Evaluate for malaria.
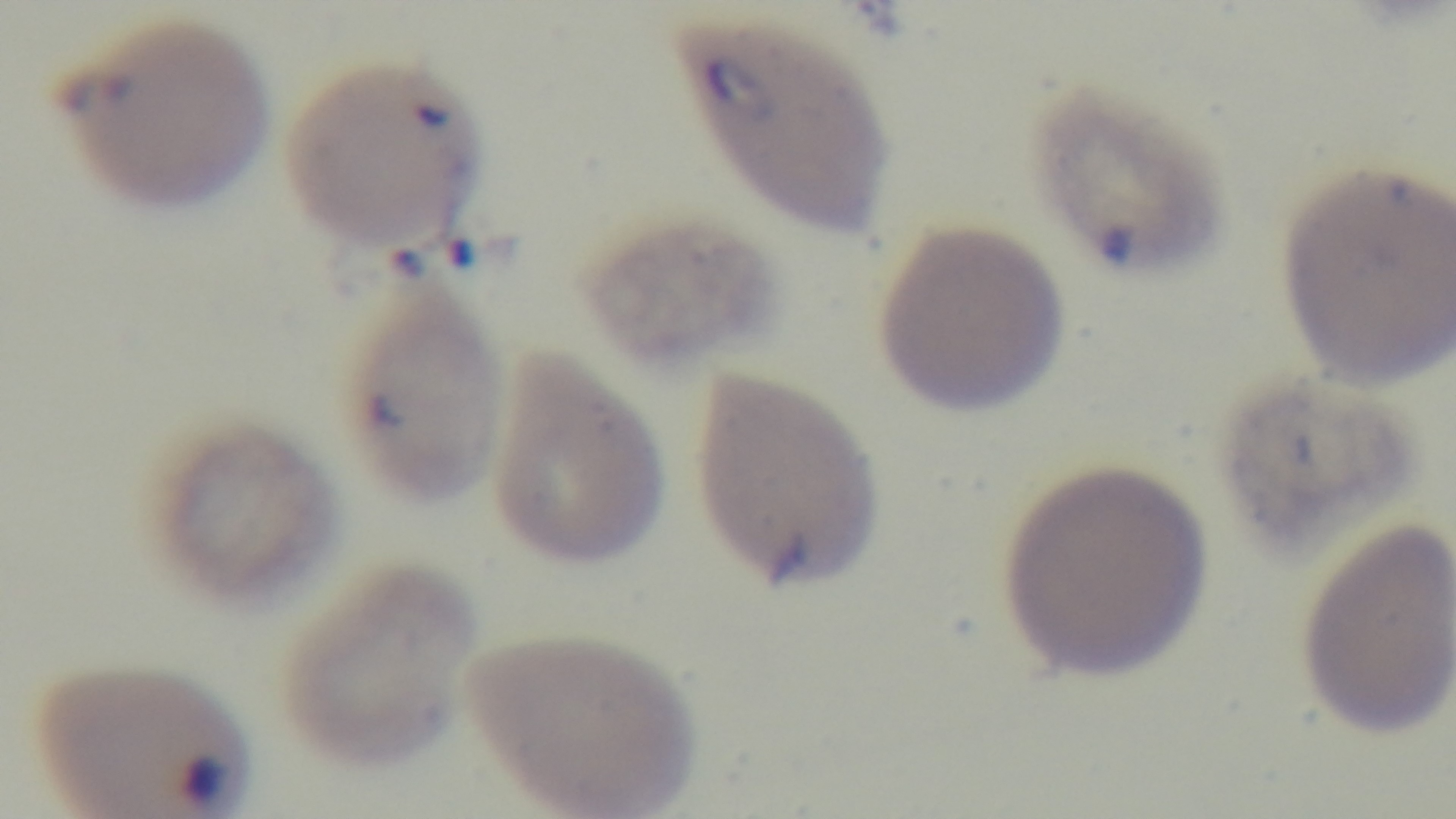
Infected.

Summary:
  - Capture: mounted 4K digital camera
  - Preparation: thin blood film
  - Stain: Giemsa
  - Field of view: one from the slide
  - Objective: 100x oil immersion
  - Modality: light microscopy